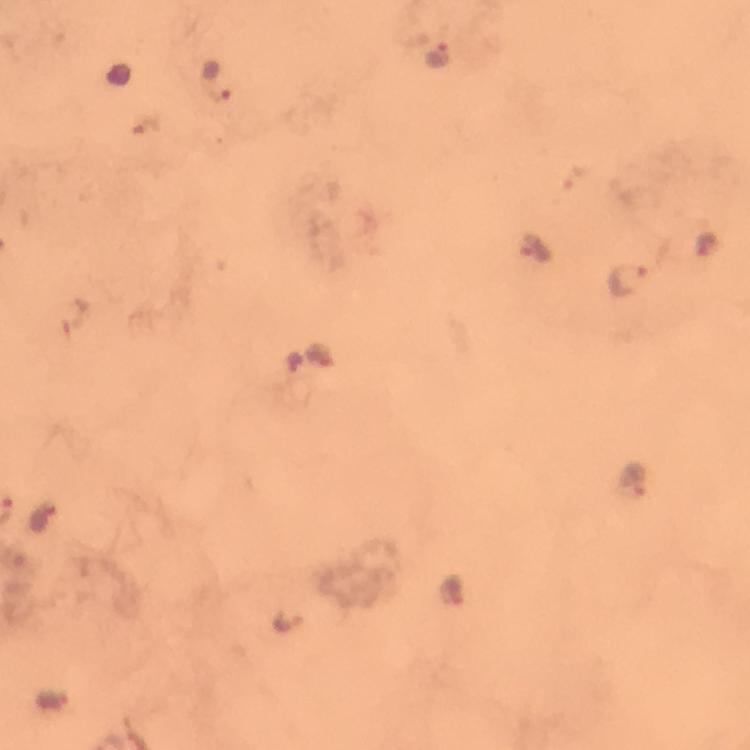

magnification = 100x
context = from a malaria diagnostic workup
stain = Giemsa
immersion oil = used
capture = smartphone photograph through a microscope
image size = 750×750 pixels
cropped from = a single field of view
preparation = thick blood film
Plasmodium parasite locations = approximate centers as (x, y) in pixels: (437, 55), (214, 80), (537, 248), (627, 280), (635, 479), (43, 518), (288, 620)